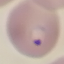

Summary:
  - Result: malaria parasites identified
  - Stain: Giemsa
  - Preparation: thin blood film
  - Capture: smartphone through the microscope eyepiece
  - Image type: automatically extracted cell patch, resized to 64 × 64 pixels